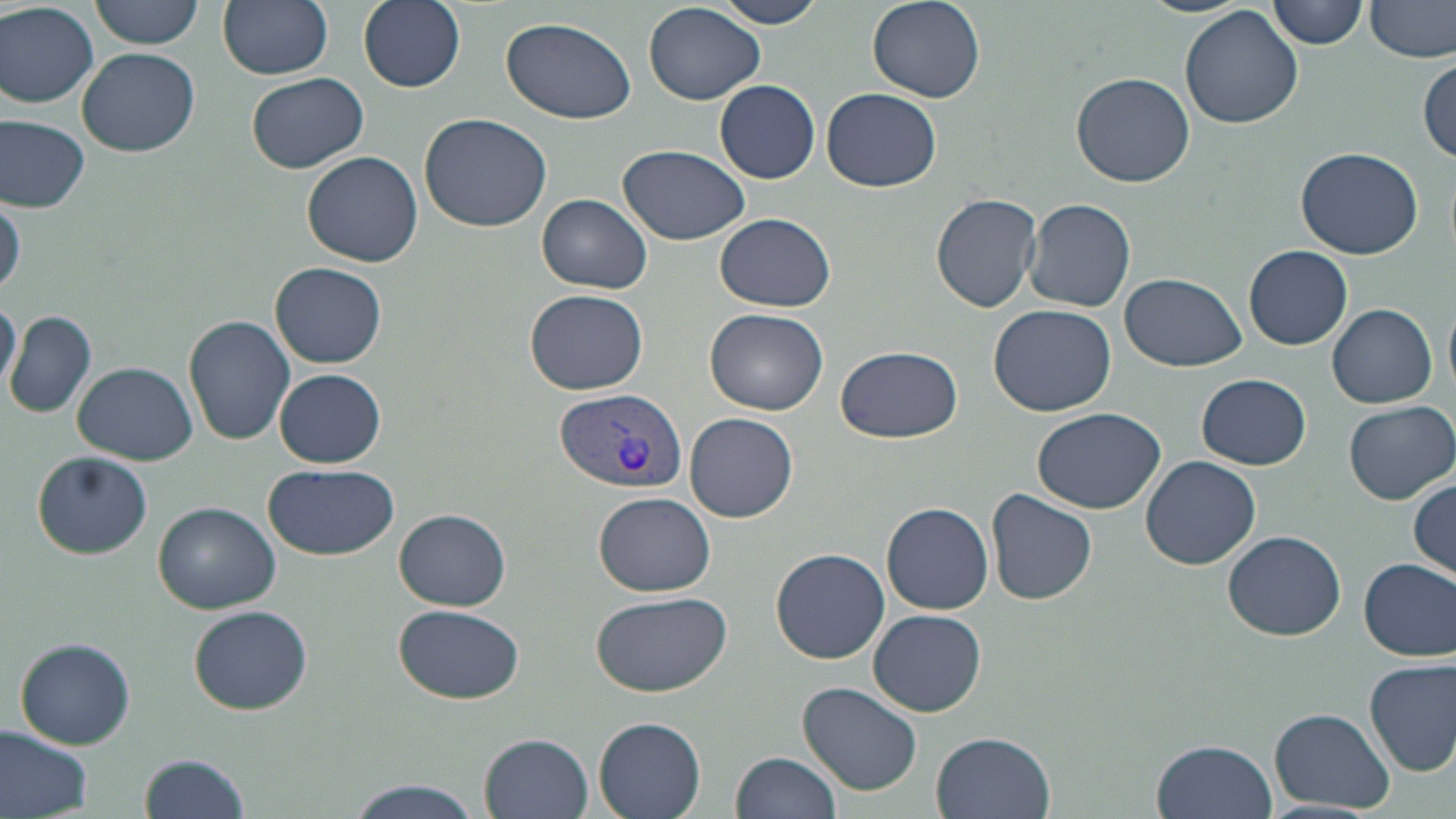

Approximate bounding boxes as (x1,y1)-(x2,y2) corner pairs in pixels. Plasmodium vivax-infected red blood cell locations: (555,386)-(686,496). Uninfected red blood cell locations: (90,0)-(205,49), (218,0)-(334,79), (358,0)-(465,92), (711,0)-(832,28), (1137,0)-(1254,17), (1268,0)-(1367,49), (1367,0)-(1456,63), (866,1)-(986,104), (0,2)-(98,108), (643,4)-(765,105), (1178,6)-(1305,132), (501,17)-(638,123), (77,47)-(201,157), (1417,56)-(1455,163), (246,72)-(368,173), (1070,72)-(1195,187), (714,80)-(821,183), (823,89)-(944,193), (419,112)-(551,233), (0,115)-(90,212), (615,146)-(753,246), (1294,147)-(1423,258), (302,151)-(424,268), (931,192)-(1043,313), (538,194)-(652,293), (1,196)-(24,299), (1024,197)-(1136,312), (714,213)-(837,312), (1244,245)-(1353,350), (271,261)-(386,368), (1122,272)-(1245,371), (525,289)-(649,396), (0,298)-(20,395), (988,304)-(1117,418), (1328,304)-(1437,408), (703,307)-(829,415), (5,310)-(97,418), (185,316)-(295,445), (835,347)-(966,444), (72,363)-(201,465), (274,368)-(386,467), (1197,372)-(1310,469), (1342,399)-(1453,505), (1031,406)-(1165,513), (684,412)-(799,523), (33,451)-(151,559), (1141,454)-(1260,569), (263,461)-(400,560), (1410,479)-(1456,577), (986,489)-(1100,605), (592,492)-(718,596), (152,501)-(281,613), (882,502)-(993,614), (395,509)-(511,610), (1223,530)-(1345,639), (771,547)-(890,663), (1358,558)-(1455,660), (588,589)-(731,697), (392,604)-(525,704), (189,606)-(314,715), (869,609)-(986,717), (15,638)-(135,749), (1365,657)-(1455,776), (798,682)-(922,795), (1271,708)-(1394,812), (592,717)-(707,818), (1,725)-(96,819), (480,732)-(594,818), (932,732)-(1055,818), (1152,738)-(1276,819), (136,750)-(251,819), (733,751)-(843,818), (340,778)-(485,818). Slide-level diagnosis: Plasmodium vivax. 1000x magnification. May-Grünwald-Giemsa stain. Image is 1456×819 pixels. Optical microscopy. Thin blood film. Single field of view.